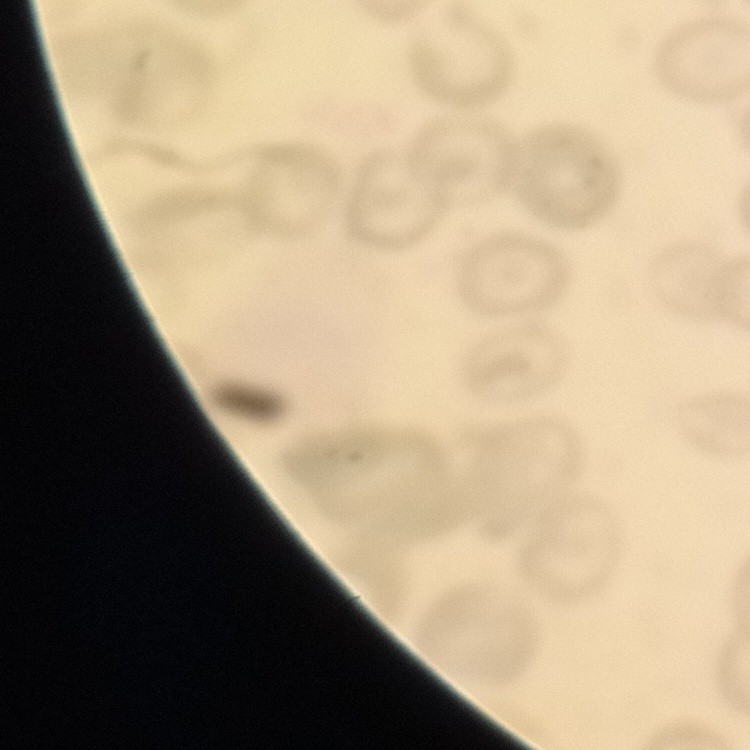
The erythrocytes exhibit no rouleaux formation. One tile cut from a larger photomicrograph. Field's or Giemsa stain. Thin peripheral smear.